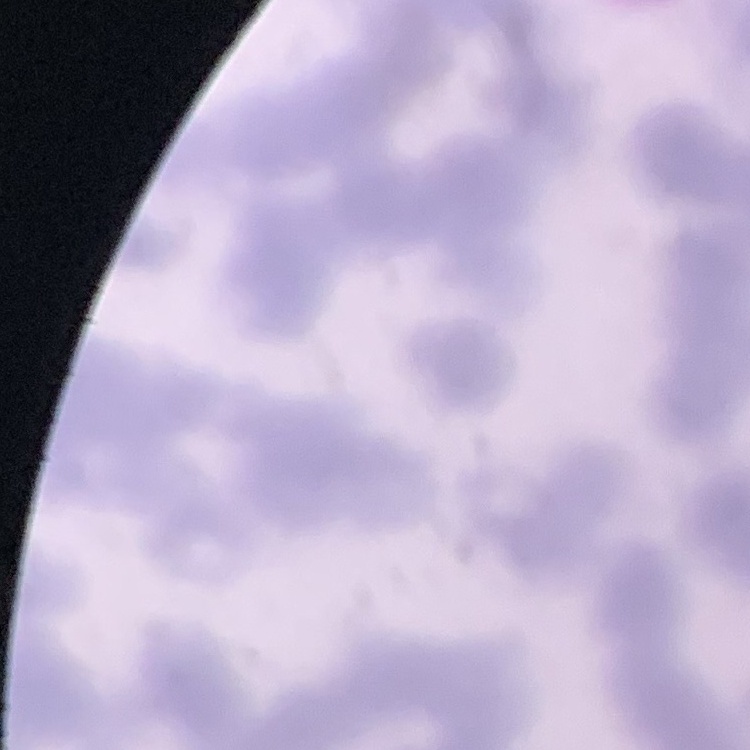 The red blood cells show rouleaux formation. One tile cut from a larger photomicrograph. Thin blood smear. Field's or Giemsa stain.